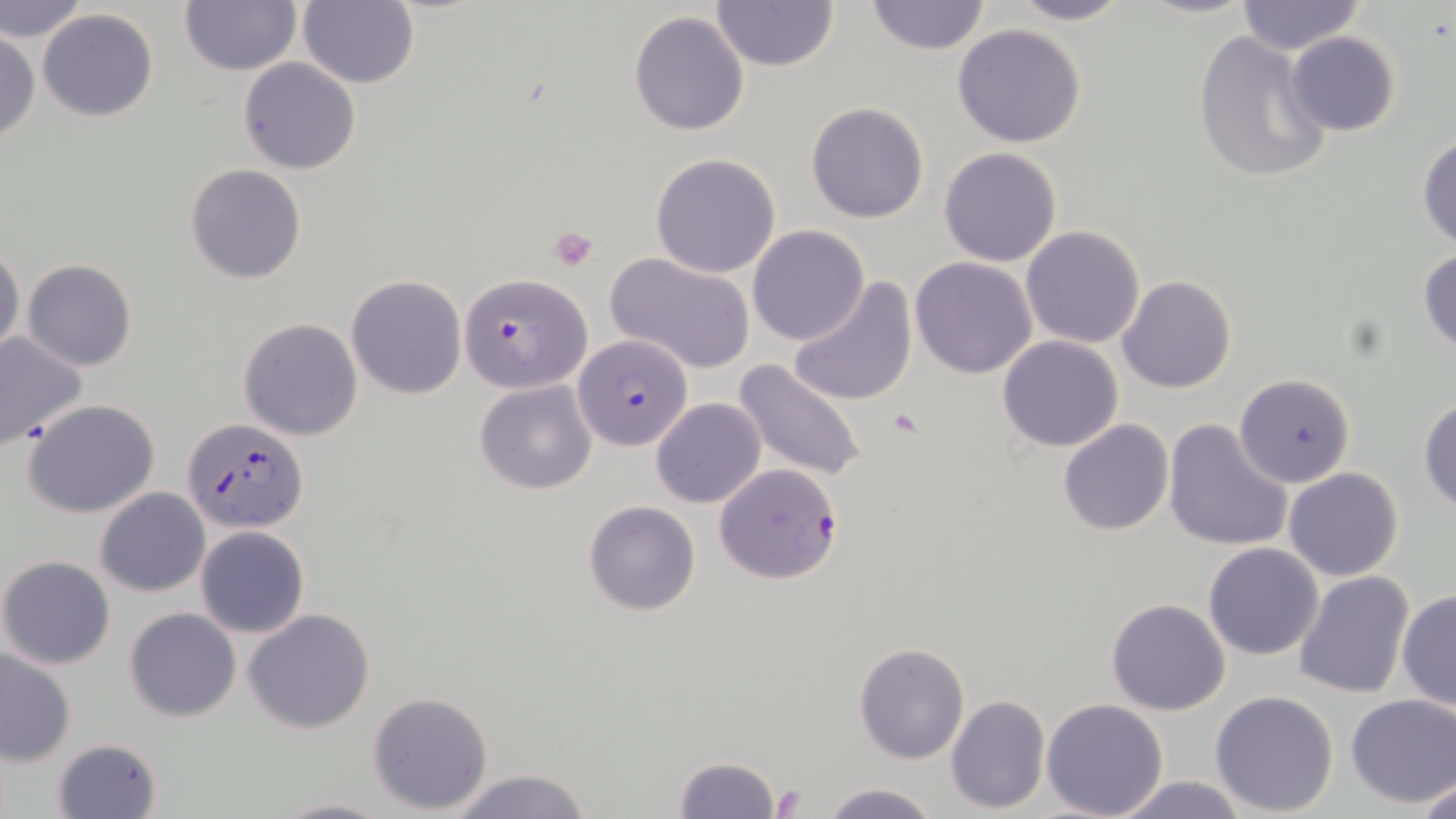

Summary:
  - Coordinate format: approximate bounding boxes as (x1,y1)-(x2,y2) corner pairs in pixels
  - Plasmodium falciparum-infected red blood cell locations: (460,273)-(592,394), (575,334)-(691,452), (180,416)-(308,533), (713,463)-(843,586)
  - Platelet locations: (548,225)-(598,270), (888,408)-(923,440), (770,784)-(805,817)
  - Uninfected red blood cell locations: (298,0)-(419,89), (1004,0)-(1134,26), (1234,0)-(1366,55), (0,1)-(90,44), (710,1)-(839,73), (862,1)-(993,55), (179,2)-(301,76), (38,9)-(159,122), (628,9)-(749,137), (952,24)-(1089,149), (1191,28)-(1334,186), (0,31)-(39,143), (1283,32)-(1402,138), (238,58)-(362,174), (806,101)-(930,223), (1416,133)-(1456,252), (939,146)-(1062,267), (649,152)-(781,277), (186,164)-(307,284), (747,225)-(869,346), (1021,226)-(1147,349), (0,241)-(23,362), (1417,250)-(1456,354), (606,253)-(755,374), (910,257)-(1038,377), (22,259)-(137,370), (346,274)-(467,399), (1116,274)-(1237,393), (786,276)-(917,408), (238,317)-(363,441), (0,330)-(90,450), (996,336)-(1123,453), (732,358)-(869,487), (1234,374)-(1355,487), (474,380)-(597,495), (1417,396)-(1456,514), (651,397)-(766,508), (23,398)-(161,519), (1163,418)-(1294,555), (1057,419)-(1174,536), (1283,467)-(1404,582), (96,488)-(210,596), (583,500)-(702,616), (195,526)-(309,639), (1204,543)-(1324,660), (0,555)-(116,669), (1292,571)-(1413,699), (1396,590)-(1455,712), (1106,598)-(1231,716), (123,607)-(242,722), (244,607)-(374,733), (854,642)-(970,764), (0,649)-(76,766), (1208,690)-(1340,816), (368,691)-(495,811), (945,694)-(1049,813), (1344,694)-(1456,808), (1041,698)-(1169,818), (50,736)-(164,819), (672,755)-(781,819), (443,769)-(595,819), (1413,772)-(1455,819), (1103,773)-(1257,818), (818,781)-(943,818), (273,795)-(392,818)
  - Slide-level diagnosis: Plasmodium falciparum
  - Magnification: 1000x
  - Preparation: thin blood film
  - Image size: 1456×819 pixels
  - Modality: optical microscopy
  - Field of view: one of a larger specimen
  - Stain: May-Grünwald-Giemsa